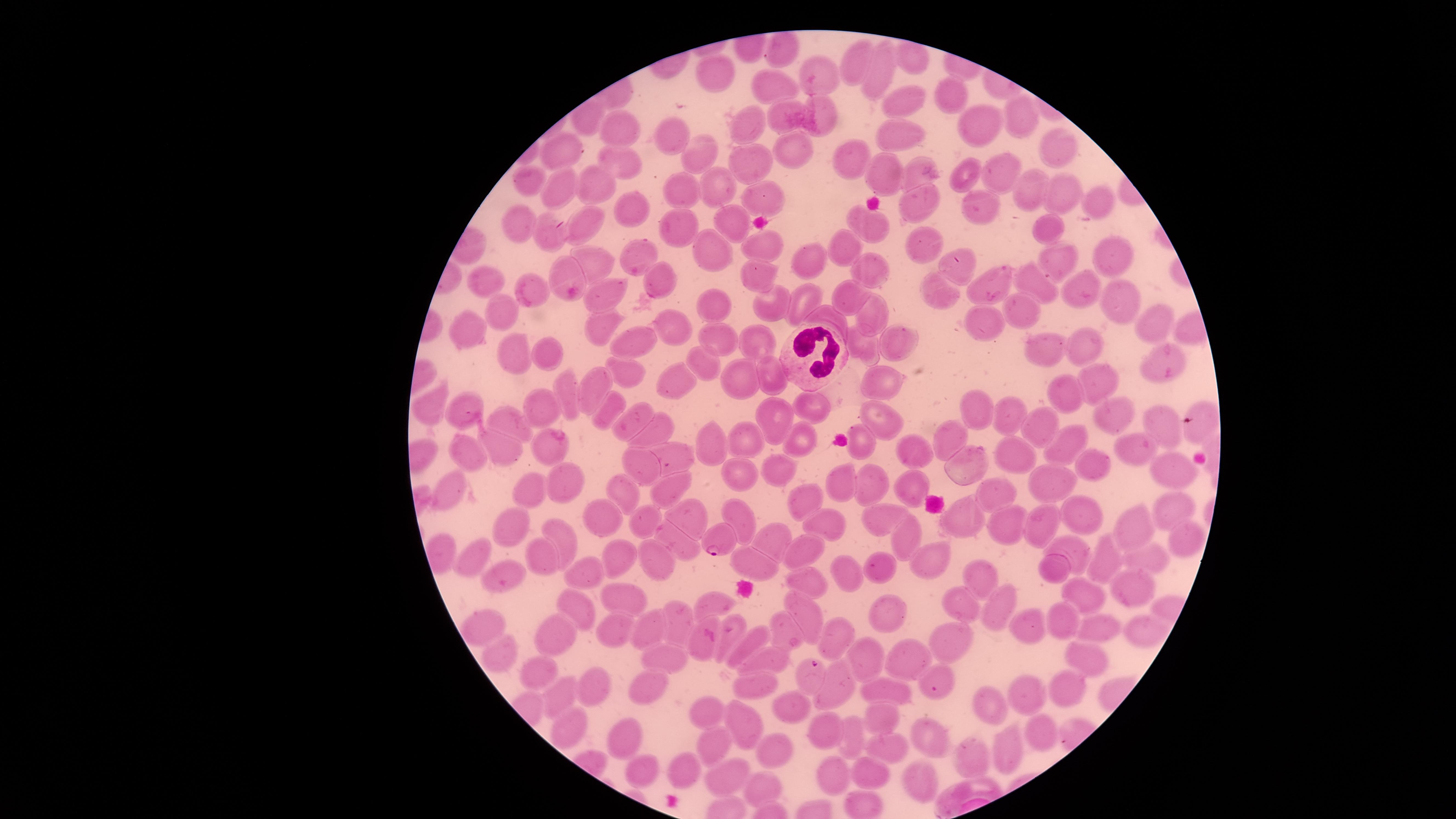

uninfected_red_blood_cells: 'approximate marker points as (x, y) in pixels: (778, 49), (853, 60), (716, 67), (815, 74), (881, 75), (769, 84), (949, 92), (906, 100), (827, 107), (784, 115), (1026, 121), (623, 123), (981, 123), (748, 124), (669, 134), (895, 134), (1062, 144), (787, 149), (564, 152), (701, 155), (847, 160), (742, 161), (623, 164), (919, 168), (969, 172), (998, 172), (876, 177), (599, 179), (527, 181), (564, 185), (717, 185), (1026, 190), (680, 191), (1056, 194), (765, 197), (913, 197), (1091, 197), (637, 206), (979, 206), (737, 217), (597, 220), (517, 221), (1052, 227), (872, 228), (680, 229), (550, 234), (923, 242), (756, 243), (714, 248), (642, 252), (847, 254), (1105, 254), (807, 258), (594, 262), (1064, 264), (864, 266), (961, 269), (566, 274), (767, 274), (485, 277), (658, 277), (988, 280), (1037, 286), (1071, 287), (529, 290), (603, 295), (803, 296), (849, 297), (941, 297), (1117, 300), (717, 305), (768, 308), (503, 309), (1028, 311), (865, 312), (831, 317), (980, 323), (1154, 324), (605, 326), (678, 327), (466, 329), (894, 338), (722, 339), (760, 342), (861, 347), (643, 348), (1073, 348), (1046, 349), (523, 352), (545, 355), (1161, 363), (698, 364), (628, 367), (738, 378), (1101, 378), (777, 379), (679, 384), (884, 384), (565, 393), (595, 394), (1061, 394), (1108, 404), (809, 405), (429, 406), (463, 408), (544, 408), (607, 409), (978, 412), (1005, 413), (883, 419), (1158, 419), (776, 422), (511, 423), (634, 423), (665, 430), (1040, 432), (952, 437), (799, 438), (750, 439), (714, 440), (1078, 441), (862, 447), (507, 448), (909, 449), (1141, 449), (469, 451), (552, 451), (670, 452), (1016, 454), (638, 461), (1094, 466), (968, 467), (745, 469), (774, 469), (1171, 470), (563, 477), (839, 480), (1058, 481), (873, 484), (676, 485), (914, 486), (451, 490), (530, 490), (988, 493), (624, 494), (805, 500), (1166, 507), (686, 514), (608, 515), (741, 516), (879, 516), (1086, 517), (648, 519), (967, 522), (1049, 522), (506, 523), (829, 524), (1009, 525), (1133, 525), (563, 534), (907, 537), (766, 539), (1186, 539), (674, 540), (805, 545), (1080, 551), (614, 553), (478, 555), (541, 555), (1144, 555), (1105, 556), (658, 558), (934, 561), (755, 563), (1056, 566), (876, 569), (511, 571), (582, 571), (808, 573), (852, 573), (978, 579), (1132, 587), (630, 591), (1080, 593), (712, 600), (575, 605), (965, 605), (806, 607), (889, 611), (1002, 611), (615, 616), (1058, 616), (678, 619), (488, 624), (1098, 624), (653, 627), (1025, 628), (736, 630), (1149, 631), (552, 632), (791, 633), (838, 634), (753, 643), (948, 645), (700, 647), (495, 651), (864, 654), (775, 655), (1088, 655), (668, 656), (902, 656), (532, 672), (751, 685), (838, 685), (1064, 685), (596, 686), (654, 686), (884, 687), (563, 694), (1031, 698), (984, 705), (792, 706), (708, 710), (743, 717), (881, 717), (569, 726), (826, 730), (1042, 732), (624, 734), (856, 734), (931, 736), (719, 743), (1011, 743), (775, 749), (881, 749), (976, 756), (646, 770), (687, 771), (864, 771), (838, 772), (726, 776), (919, 776), (761, 788), (979, 788)'
white_blood_cells: 'approximate marker points as (x, y) in pixels: (808, 350)'
field_of_view: single
capture: smartphone photograph through the microscope eyepiece
stain: Giemsa
presence: malaria parasites detected
visible_region: circular
image_size: 1456×819 pixels
species: Plasmodium falciparum
parasitized_red_blood_cells: 'approximate marker points as (x, y) in pixels: (717, 539), (808, 676), (937, 682)'
preparation: thin blood film